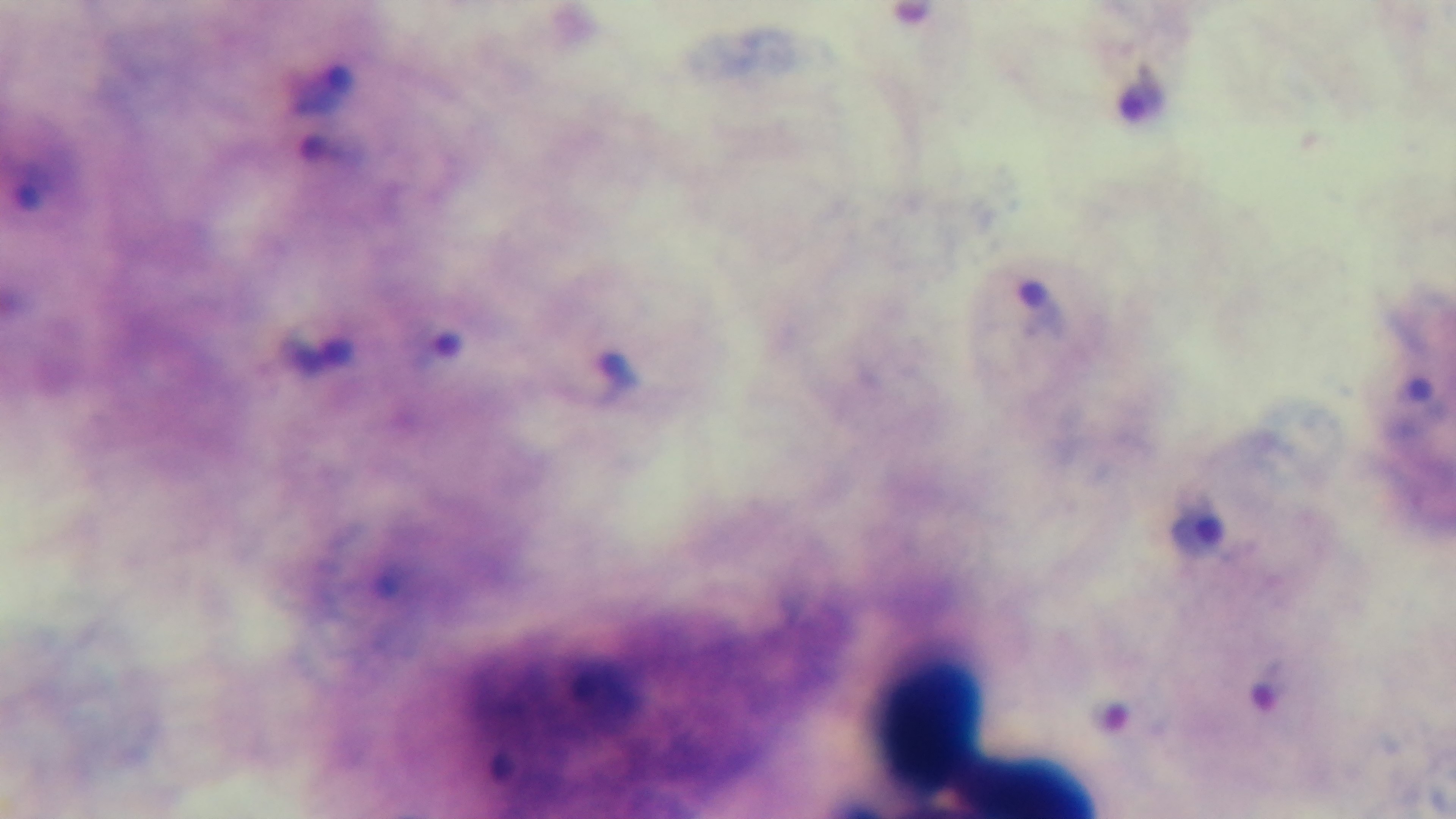

malaria status = positive
field of view = single
modality = light microscopy
stain = Giemsa
preparation = thick smear
capture = mounted 4K digital camera
objective = 100x oil immersion